Point out malaria parasites and leukocytes.
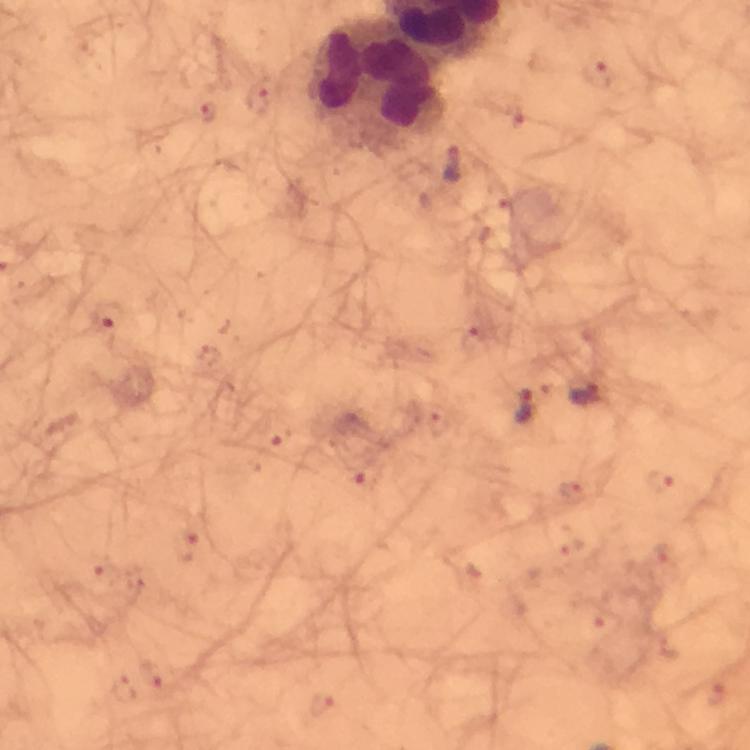
Approximate object centers, in pixels from the top-left corner.
Malaria parasites: (x=595, y=75), (x=258, y=100), (x=206, y=114), (x=514, y=117), (x=451, y=167), (x=498, y=212), (x=105, y=316), (x=474, y=342), (x=587, y=396), (x=523, y=406), (x=438, y=424), (x=277, y=436), (x=367, y=478), (x=661, y=481), (x=574, y=494), (x=188, y=540), (x=571, y=546), (x=661, y=553), (x=105, y=575), (x=603, y=618), (x=152, y=676), (x=123, y=688), (x=717, y=694), (x=321, y=706).
Leukocytes: (x=377, y=82).

Summary:
  - Stain: Giemsa
  - Preparation: thick blood smear
  - Immersion oil: used
  - Image size: 750×750 pixels
  - Capture: smartphone photograph through a microscope
  - Cropped from: a single field of view
  - Magnification: 100x
  - Context: from a diagnostic examination for malaria